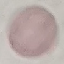
Result: no malaria parasites seen. Giemsa-stained preparation. Photographed with a smartphone camera at the microscope eyepiece. Thin blood film. Cell patch, automatically extracted from a larger field of view and resized to 64 × 64 pixels.